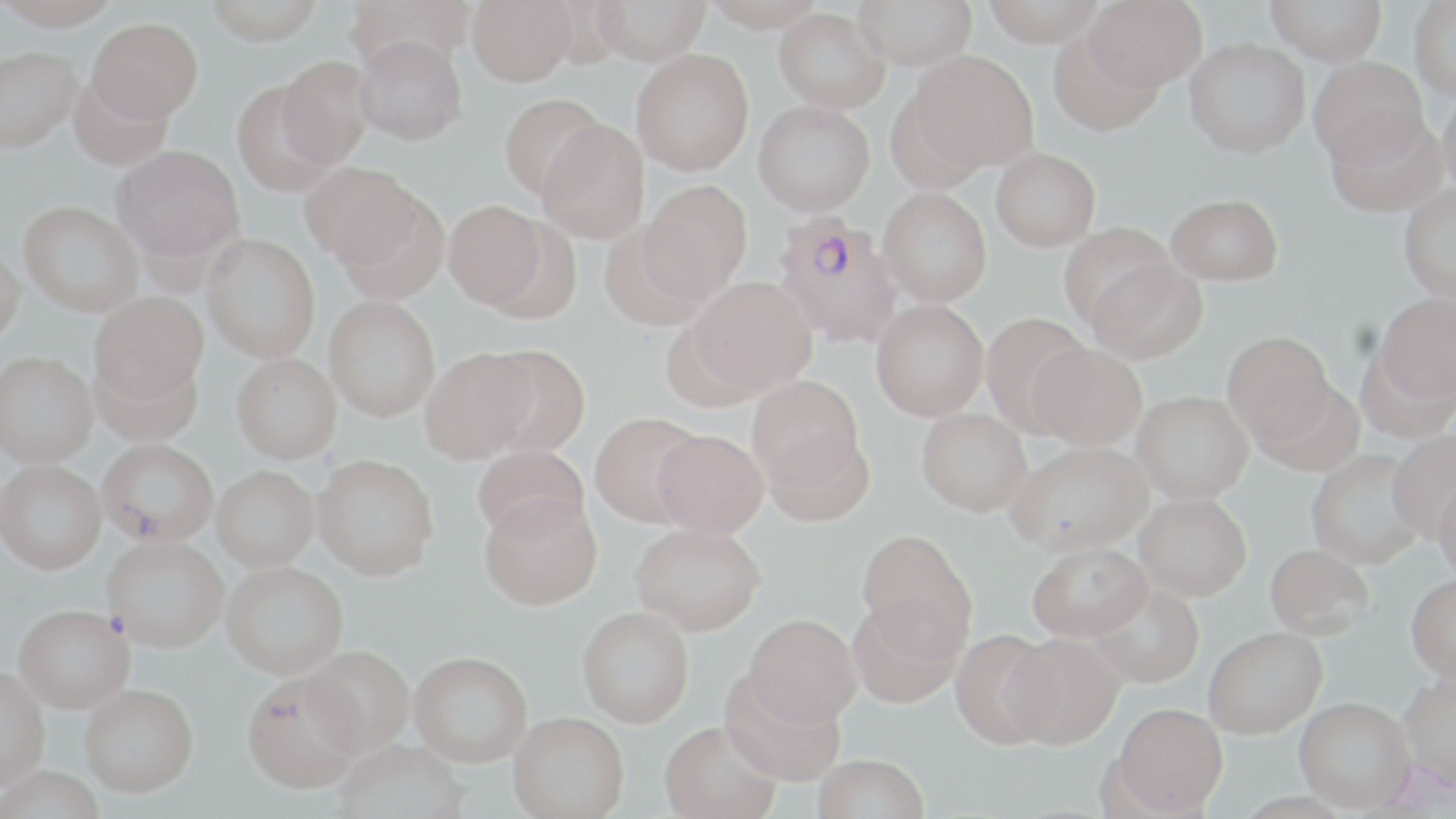
Summary:
  - Coordinate format: approximate bounding boxes as [x1, y1, x2, y2] in pixels
  - Plasmodium falciparum-infected red blood cell locations: [772, 211, 905, 349]
  - Uninfected red blood cell locations: [0, 0, 122, 29], [204, 0, 324, 44], [344, 0, 474, 73], [466, 0, 577, 85], [592, 0, 710, 66], [699, 0, 826, 32], [853, 0, 977, 70], [980, 0, 1106, 46], [1084, 0, 1206, 91], [1264, 0, 1387, 66], [1410, 1, 1456, 102], [773, 7, 890, 113], [87, 17, 203, 122], [1048, 30, 1163, 134], [354, 34, 467, 145], [1184, 37, 1309, 158], [0, 45, 81, 154], [631, 49, 754, 175], [910, 51, 1039, 172], [277, 55, 376, 167], [1309, 56, 1428, 169], [68, 73, 175, 171], [230, 81, 340, 198], [1438, 89, 1456, 200], [498, 93, 606, 200], [753, 100, 875, 216], [1324, 111, 1448, 217], [537, 119, 649, 245], [112, 145, 244, 266], [991, 147, 1101, 251], [299, 162, 420, 267], [639, 180, 753, 300], [1398, 184, 1456, 303], [329, 185, 449, 305], [878, 187, 992, 306], [1166, 193, 1283, 285], [18, 200, 143, 316], [443, 200, 548, 309], [483, 212, 581, 321], [1058, 222, 1176, 331], [598, 224, 708, 331], [202, 233, 320, 362], [0, 242, 26, 348], [1087, 258, 1207, 363], [689, 276, 816, 394], [88, 291, 209, 406], [1375, 292, 1456, 403], [324, 295, 440, 422], [870, 300, 989, 420], [980, 313, 1092, 434], [1222, 331, 1336, 445], [1028, 342, 1147, 449], [479, 345, 590, 457], [421, 347, 537, 463], [1357, 347, 1455, 445], [90, 352, 204, 448], [0, 353, 98, 470], [230, 353, 343, 466], [747, 376, 864, 490], [1253, 380, 1366, 475], [1131, 390, 1253, 504], [917, 407, 1032, 516], [590, 412, 706, 527], [652, 429, 769, 538], [763, 429, 874, 528], [1387, 431, 1456, 538], [1007, 441, 1152, 555], [97, 442, 218, 552], [472, 445, 588, 541], [1306, 449, 1428, 570], [312, 454, 438, 581], [0, 463, 106, 579], [211, 469, 319, 575], [1433, 480, 1456, 583], [479, 492, 602, 611], [1134, 493, 1252, 600], [630, 522, 766, 636], [857, 528, 977, 656], [103, 540, 228, 656], [1027, 541, 1152, 641], [1264, 544, 1374, 640], [221, 565, 348, 683], [1405, 574, 1456, 681], [1087, 582, 1204, 688], [847, 596, 964, 709], [577, 606, 694, 729], [12, 609, 133, 718], [744, 613, 862, 728], [1203, 627, 1327, 738], [950, 629, 1059, 749], [1003, 633, 1124, 749], [303, 648, 415, 762], [409, 654, 532, 772], [0, 670, 49, 795], [720, 671, 846, 787], [1398, 672, 1456, 792], [243, 677, 365, 798], [80, 689, 199, 803], [1294, 697, 1416, 813], [1112, 704, 1228, 816], [507, 716, 629, 819], [659, 724, 782, 819], [334, 743, 469, 819], [812, 755, 930, 819], [0, 771, 104, 819]
  - Slide-level diagnosis: Plasmodium falciparum
  - Field of view: one of a larger specimen
  - Image size: 1456×819 pixels
  - Stain: May-Grünwald-Giemsa
  - Modality: optical microscopy
  - Magnification: 1000x
  - Preparation: thin blood smear